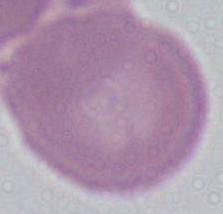

modality = micrograph
identification = red blood cell
magnification = 1000x